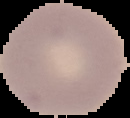 Malaria status: uninfected. Image is 130×118 pixels. Segmented cell region on a black background. From a thin blood film.